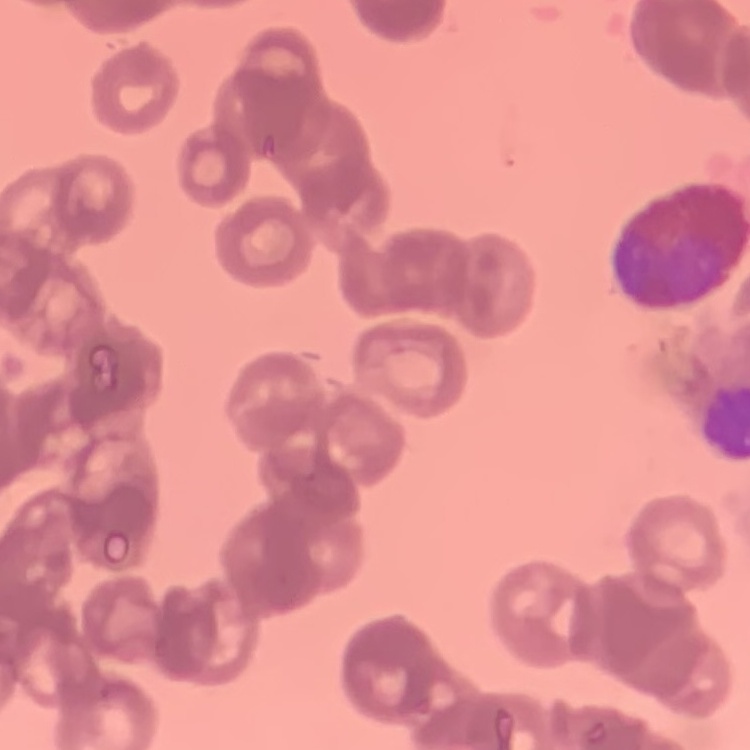

erythrocyte morphology = rouleaux formation
image type = one tile cut from a larger photomicrograph
stain = Field's or Giemsa
preparation = thin blood smear